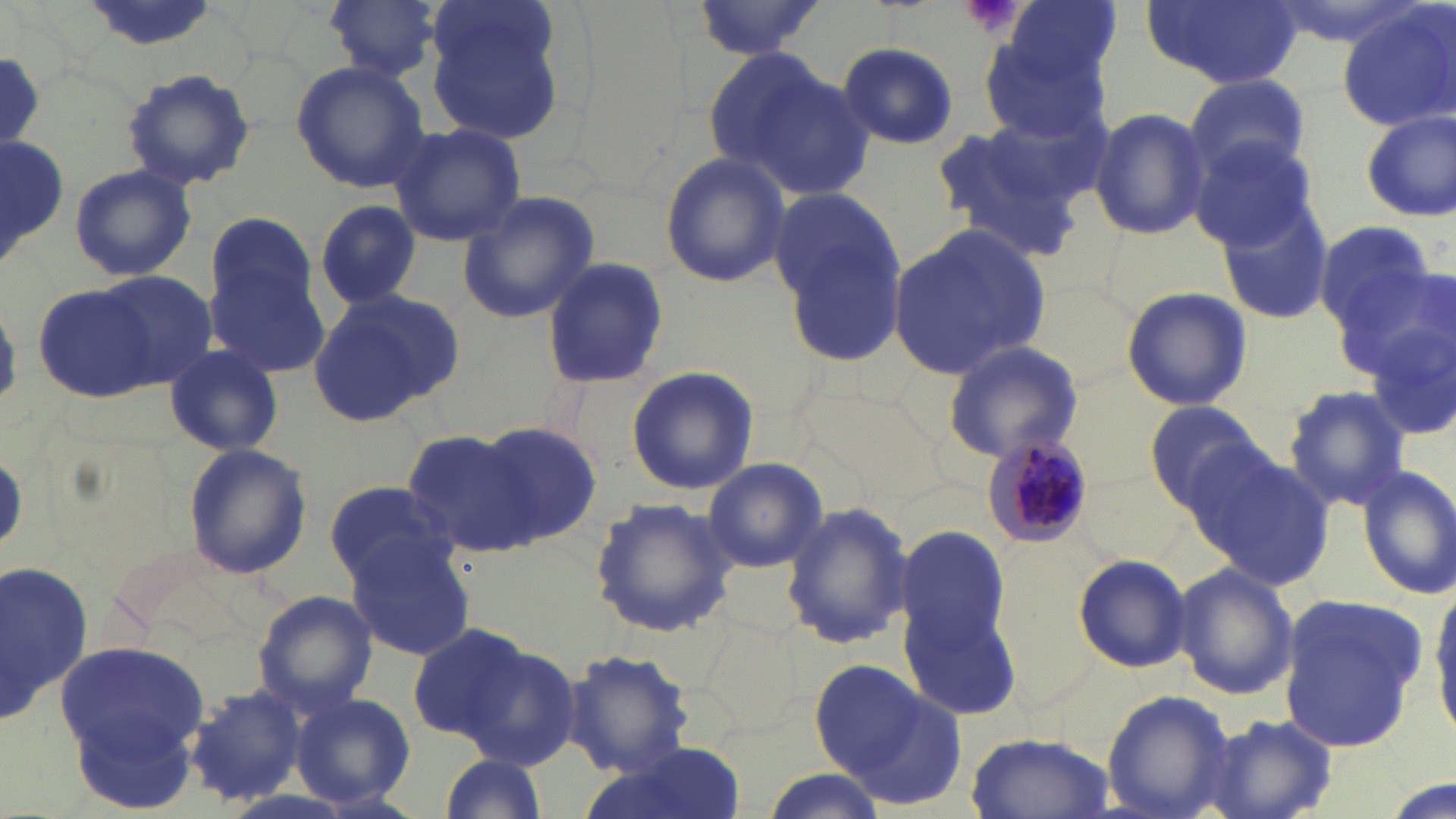
Approximate bounding boxes as (x1,y1)-(x2,y2) corner pairs in pixels. Platelet locations: (958,0)-(1026,40). Uninfected red blood cell locations: (80,0)-(227,52), (324,0)-(443,83), (688,0)-(831,63), (1004,0)-(1123,87), (420,1)-(572,145), (1146,1)-(1298,89), (1337,3)-(1456,133), (980,36)-(1111,148), (840,42)-(958,147), (706,45)-(868,194), (291,60)-(428,192), (120,69)-(256,191), (1183,74)-(1314,186), (1090,106)-(1211,241), (1358,110)-(1455,223), (927,118)-(1090,262), (387,123)-(527,247), (0,131)-(72,277), (1189,136)-(1321,253), (658,151)-(789,288), (69,164)-(197,281), (767,186)-(910,370), (1217,187)-(1337,327), (456,192)-(601,323), (315,200)-(421,310), (202,212)-(320,341), (1312,220)-(1439,341), (888,225)-(1051,380), (1342,251)-(1451,387), (541,258)-(669,392), (207,267)-(330,375), (98,270)-(216,390), (32,284)-(159,403), (1121,284)-(1252,413), (307,290)-(463,428), (1368,317)-(1456,448), (938,339)-(1087,465), (163,343)-(284,457), (625,366)-(759,496), (1283,384)-(1411,513), (1145,399)-(1268,512), (475,423)-(604,541), (401,429)-(540,557), (1187,441)-(1334,590), (182,443)-(313,580), (699,458)-(831,574), (1356,465)-(1456,600), (322,481)-(457,587), (589,497)-(738,637), (779,501)-(914,652), (894,522)-(1020,699), (344,535)-(476,659), (1072,553)-(1192,674), (0,556)-(96,734), (1171,562)-(1299,700), (1428,583)-(1456,738), (253,589)-(379,713), (1277,594)-(1428,746), (406,623)-(528,743), (700,623)-(802,738), (58,641)-(211,786), (461,642)-(581,771), (561,651)-(696,776), (812,661)-(963,800), (187,688)-(306,807), (1102,689)-(1237,819), (290,693)-(418,810), (70,702)-(206,814), (1193,712)-(1337,819), (963,731)-(1118,818), (586,748)-(745,819), (435,752)-(548,819), (755,770)-(890,819). Plasmodium malariae-infected red blood cell locations: (982,434)-(1096,550). White blood cell locations: (2,550)-(94,740). Slide-level diagnosis: Plasmodium malariae. May-Grünwald-Giemsa-stained preparation. One field of a larger specimen. Optical microscopy. Thin blood smear. 1000x magnification. Image is 1456×819 pixels.